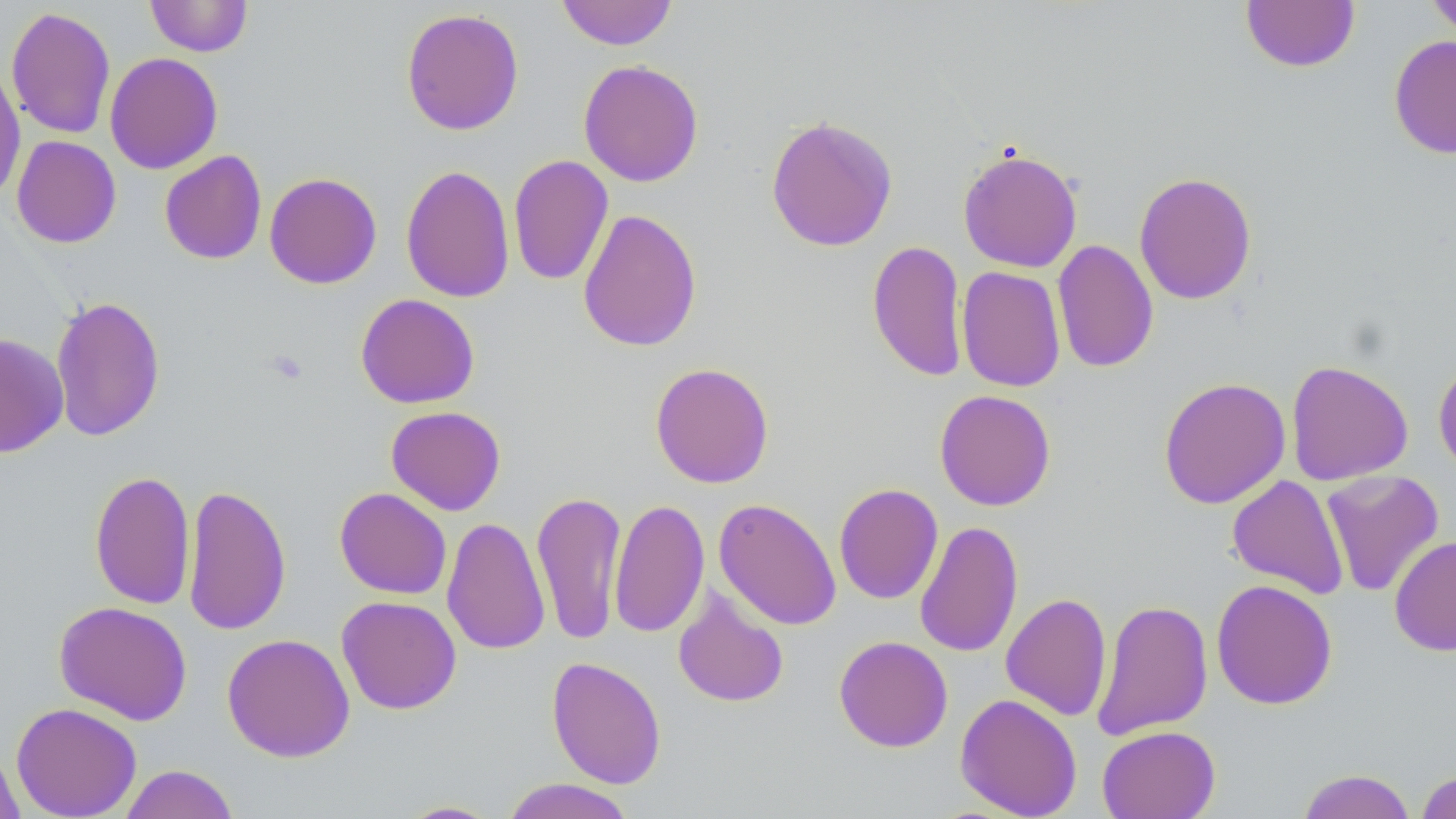
Summary:
  - Coordinate format: approximate bounding boxes as [x1, y1, x2, y2] in pixels
  - Uninfected red blood cell locations: [144, 0, 253, 57], [556, 0, 678, 50], [1241, 0, 1361, 73], [1424, 0, 1456, 40], [6, 6, 116, 140], [400, 8, 524, 136], [1388, 34, 1456, 160], [105, 53, 223, 174], [578, 59, 704, 187], [0, 63, 26, 203], [765, 114, 898, 252], [12, 136, 121, 248], [957, 146, 1083, 273], [159, 150, 267, 265], [508, 154, 614, 286], [400, 164, 515, 303], [1134, 171, 1257, 305], [264, 172, 382, 289], [577, 207, 702, 353], [1051, 239, 1158, 373], [868, 240, 968, 382], [956, 266, 1065, 392], [355, 293, 480, 409], [50, 295, 165, 443], [10, 318, 129, 453], [0, 333, 68, 458], [1433, 358, 1456, 475], [1286, 359, 1413, 485], [650, 362, 775, 489], [1158, 377, 1291, 509], [935, 389, 1056, 511], [385, 406, 506, 515], [1320, 469, 1445, 598], [89, 470, 196, 610], [1226, 474, 1349, 599], [182, 483, 292, 636], [833, 483, 943, 605], [334, 487, 452, 600], [531, 489, 626, 645], [713, 497, 842, 631], [609, 499, 709, 638], [441, 516, 550, 656], [914, 520, 1023, 658], [1389, 535, 1456, 656], [1211, 579, 1338, 710], [673, 586, 789, 708], [1001, 592, 1112, 721], [336, 595, 462, 715], [1092, 598, 1213, 741], [54, 601, 193, 725], [222, 633, 355, 762], [833, 635, 953, 752], [546, 656, 667, 789], [955, 693, 1082, 818], [11, 702, 142, 818], [1097, 725, 1220, 819], [0, 743, 24, 819], [118, 763, 239, 819], [1296, 768, 1417, 819], [1416, 770, 1456, 819], [500, 778, 637, 819], [396, 799, 502, 818]
  - Slide-level diagnosis: negative for blood parasites
  - Field of view: one of a larger specimen
  - Stain: May-Grünwald-Giemsa
  - Preparation: thin blood smear
  - Modality: optical microscopy
  - Magnification: 1000x
  - Image size: 1456×819 pixels